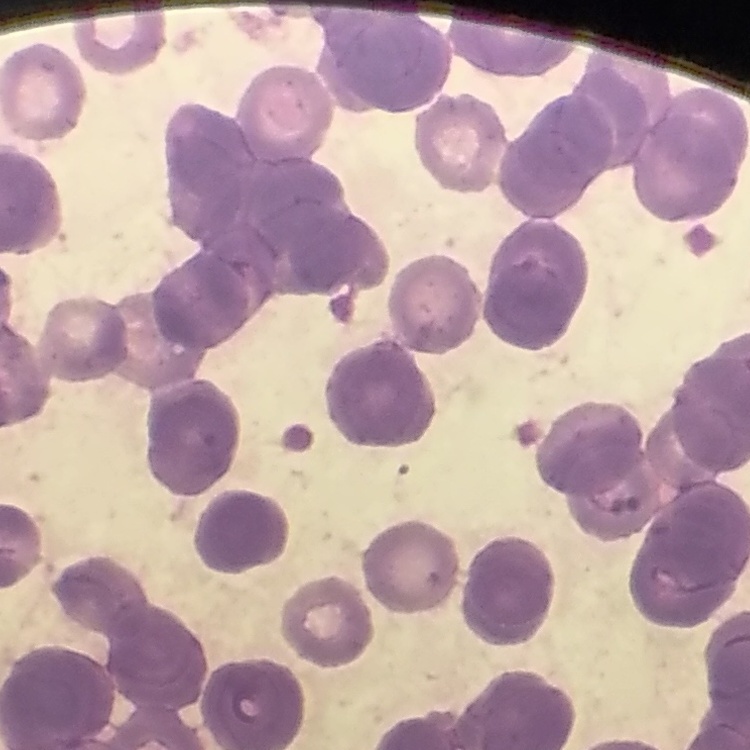

The erythrocytes exhibit rouleaux formation. Field's or Giemsa stain. Thin blood film. One tile cut from a larger photomicrograph.